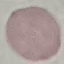

Result: no malaria parasites detected. Automatically extracted cell patch, resized to 64 × 64 pixels. Thin blood smear. Giemsa-stained preparation. Acquired by smartphone through the microscope eyepiece.